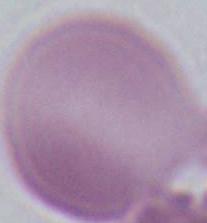

{
  "magnification": "1000x",
  "identification": "red blood cell",
  "modality": "micrograph"
}